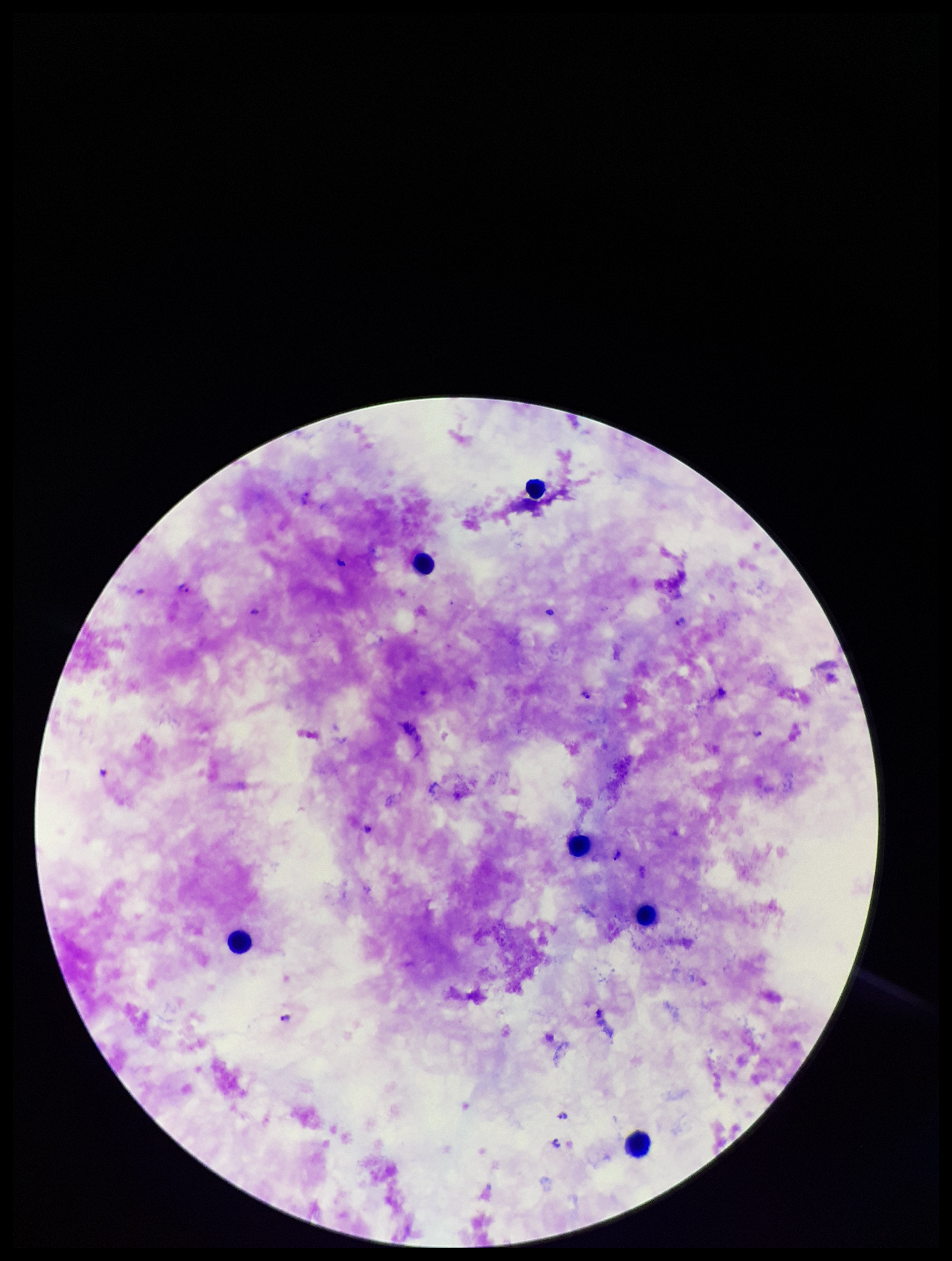
Single field of view. Plasmodium parasites: seen. Patient malaria status: infected. Leukocyte count: 6. Preparation: thick blood smear. Species reported for this patient: Plasmodium falciparum. Parasite count: 11. Photographed through the microscope eyepiece with a smartphone camera. Image is 952×1261 pixels. Giemsa stain.